Name the blood parasite species.
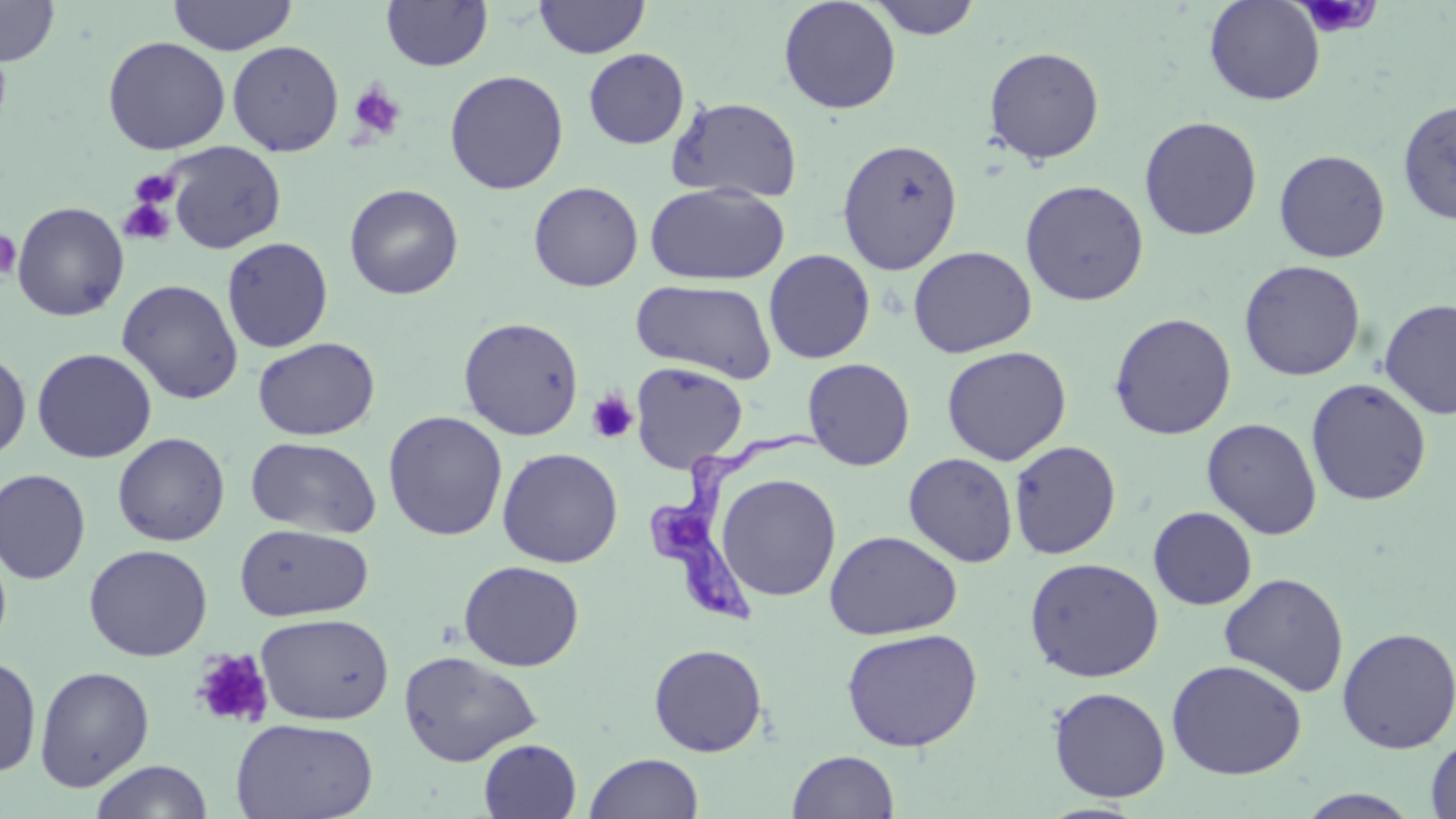

Trypanosoma brucei.

Approximate bounding boxes as [x1, y1, x2, y2] in pixels. Platelet locations (subset): [1295, 0, 1382, 39], [348, 82, 406, 141], [129, 169, 181, 209], [118, 199, 175, 246], [0, 229, 21, 281], [586, 391, 638, 444]. Trypanosoma brucei locations: [649, 416, 824, 635]. Uninfected red blood cell locations (subset): [167, 0, 297, 55], [534, 0, 649, 59], [778, 0, 902, 114], [866, 0, 983, 39], [1204, 0, 1325, 105], [0, 1, 60, 66], [380, 1, 493, 71], [102, 35, 230, 155], [227, 40, 344, 157], [983, 46, 1105, 164], [583, 48, 689, 149], [444, 70, 568, 194], [667, 96, 803, 203], [1397, 98, 1456, 225], [1138, 115, 1262, 241], [837, 138, 964, 275], [163, 140, 287, 254], [1273, 149, 1391, 263], [1020, 179, 1149, 306], [528, 181, 644, 292], [344, 183, 464, 300], [645, 183, 790, 286], [10, 201, 129, 322], [221, 236, 333, 353], [908, 245, 1036, 358], [763, 249, 876, 364], [1239, 260, 1366, 381], [117, 278, 244, 404], [631, 279, 778, 382], [1379, 298, 1456, 420], [1109, 312, 1237, 439], [458, 316, 584, 440], [252, 337, 380, 440], [941, 345, 1072, 465], [31, 347, 157, 463], [0, 350, 32, 462], [802, 357, 915, 471], [630, 361, 748, 473], [1305, 378, 1432, 506], [383, 411, 507, 541], [1201, 417, 1322, 540], [112, 432, 230, 546], [245, 436, 382, 538], [1008, 440, 1121, 560], [497, 447, 623, 567], [904, 452, 1018, 567], [0, 468, 91, 585], [716, 473, 841, 601], [1148, 506, 1257, 610], [234, 523, 374, 621], [823, 530, 962, 640], [0, 536, 13, 661], [83, 544, 213, 661], [1024, 556, 1164, 682], [458, 560, 585, 671], [1219, 572, 1350, 697], [255, 613, 394, 725], [1336, 626, 1456, 754], [840, 627, 983, 752], [648, 642, 768, 757], [400, 650, 542, 766], [0, 654, 41, 778], [1166, 659, 1307, 780], [34, 665, 155, 792], [1047, 686, 1171, 803], [231, 717, 379, 819], [1425, 734, 1456, 819], [479, 738, 582, 818], [787, 750, 899, 818], [584, 752, 704, 819], [89, 760, 214, 819], [1295, 789, 1425, 818]. May-Grünwald-Giemsa-stained preparation. Thin blood smear. Optical microscopy. 1000x magnification. One field of a larger specimen. Image is 1456×819 pixels.